Describe the morphology of the erythrocytes.
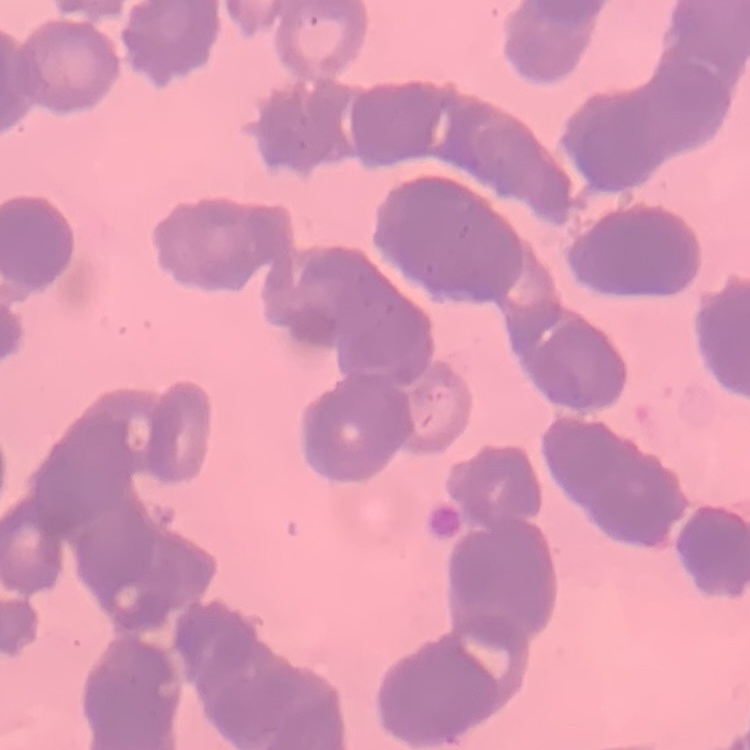
Rouleaux formation.

stain = Field's or Giemsa
preparation = thin blood smear
image type = square crop of a larger photomicrograph